Classify this cell by malaria status.
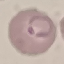
Parasitized.

Summary:
  - Image type: cell patch, automatically extracted from a larger field of view and resized to 64 × 64 pixels
  - Preparation: thin smear
  - Capture: smartphone through the microscope eyepiece
  - Stain: Giemsa